Outline each blood parasite and name the species.
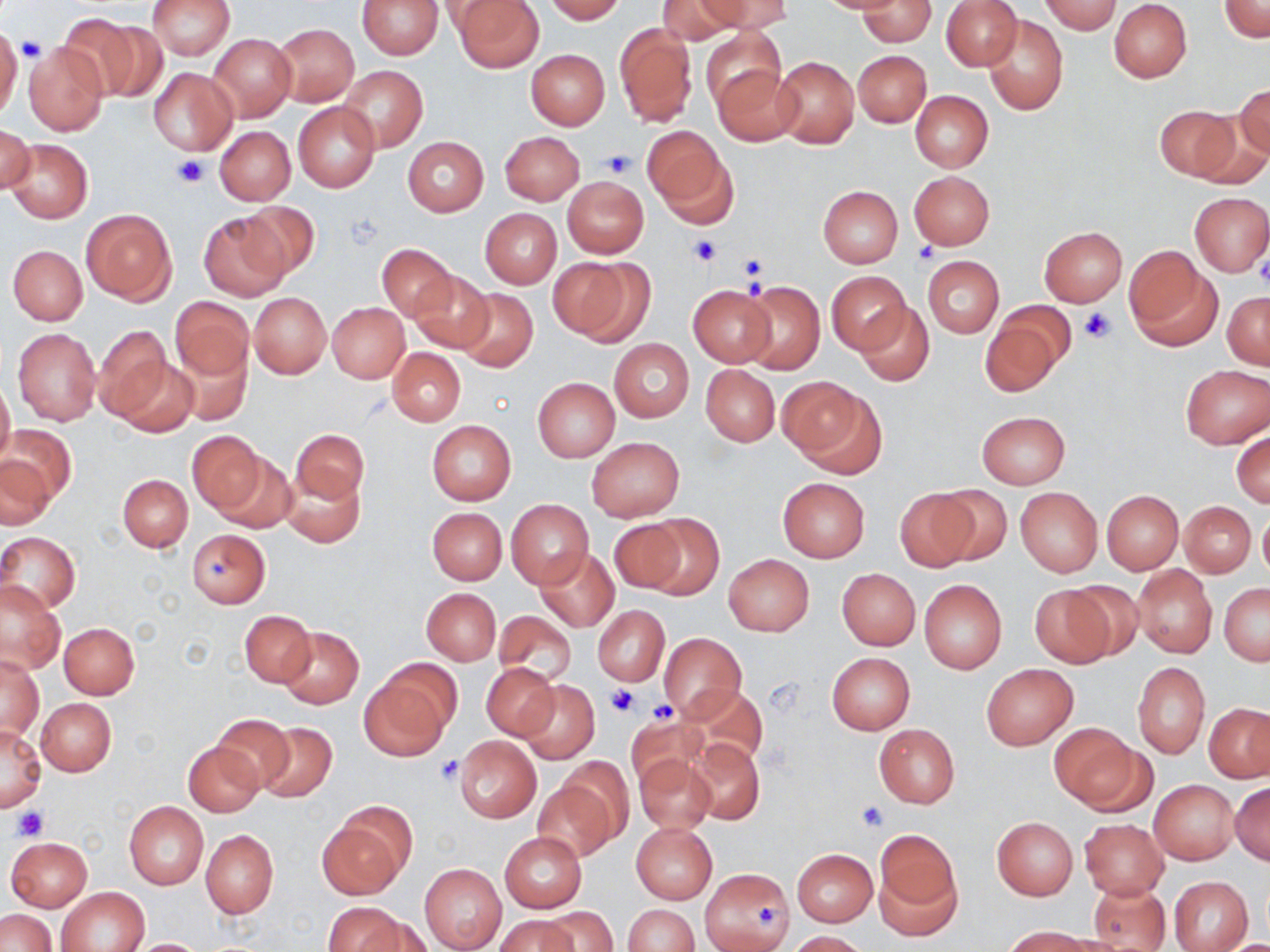

No blood parasites observed.

slide_level_diagnosis: negative for blood parasites
magnification: 1000x
stain: May-Grünwald-Giemsa
modality: light microscopy
image_size: 1270×952 pixels
uninfected_red_blood_cell_locations: 'approximate bounding boxes as [x1, y1, x2, y2] in pixels: [147, 0, 235, 59], [356, 0, 443, 59], [543, 0, 625, 22], [655, 0, 741, 44], [702, 0, 792, 34], [815, 0, 913, 15], [1041, 0, 1122, 35], [453, 1, 543, 71], [858, 1, 936, 48], [941, 1, 1021, 71], [1108, 1, 1193, 82], [1220, 1, 1269, 42], [57, 14, 144, 99], [982, 15, 1068, 116], [93, 23, 172, 101], [614, 23, 697, 126], [272, 24, 359, 105], [0, 26, 22, 119], [701, 26, 786, 113], [209, 34, 296, 121], [22, 43, 108, 136], [526, 49, 609, 129], [853, 50, 931, 127], [770, 54, 859, 150], [710, 64, 800, 146], [341, 66, 427, 152], [149, 68, 236, 153], [1234, 84, 1269, 163], [910, 90, 993, 173], [293, 102, 379, 192], [1154, 105, 1241, 181], [1, 125, 33, 196], [215, 126, 296, 205], [641, 127, 729, 220], [499, 131, 583, 205], [402, 137, 488, 216], [5, 138, 92, 223], [909, 171, 994, 249], [562, 176, 649, 258], [818, 185, 902, 267], [1189, 193, 1270, 276], [236, 200, 320, 281], [81, 208, 177, 306], [480, 208, 561, 287], [198, 212, 288, 300], [1038, 226, 1127, 307], [377, 243, 455, 322], [8, 245, 87, 325], [1125, 250, 1221, 351], [923, 256, 1004, 338], [557, 257, 654, 347], [408, 269, 495, 354], [827, 270, 910, 354], [738, 280, 825, 375], [686, 284, 777, 368], [455, 288, 538, 371], [1223, 291, 1270, 369], [249, 293, 331, 378], [169, 297, 253, 380], [855, 302, 933, 386], [328, 303, 410, 382], [981, 306, 1068, 394], [92, 324, 171, 420], [12, 327, 101, 426], [609, 339, 694, 421], [171, 341, 253, 423], [387, 347, 465, 425], [114, 357, 200, 438], [700, 365, 779, 447], [1180, 365, 1269, 448], [533, 377, 619, 461], [777, 377, 875, 462], [0, 379, 14, 471], [976, 409, 1071, 489], [427, 421, 517, 506], [3, 424, 75, 507], [293, 428, 369, 505], [1232, 428, 1269, 508], [187, 431, 265, 514], [587, 437, 684, 522], [215, 452, 298, 535], [0, 455, 53, 530], [281, 468, 364, 548], [118, 474, 193, 552], [778, 477, 869, 562], [934, 485, 1011, 564], [1016, 487, 1102, 576], [893, 489, 980, 572], [1101, 490, 1183, 574], [507, 499, 592, 588], [1180, 502, 1255, 576], [427, 506, 506, 584], [1258, 508, 1270, 583], [638, 514, 724, 596], [609, 518, 685, 593], [185, 528, 271, 608], [0, 531, 81, 613], [534, 546, 620, 632], [723, 554, 813, 636], [1132, 565, 1217, 659], [836, 568, 920, 649], [919, 578, 1007, 674], [1, 581, 65, 673], [1063, 581, 1144, 661], [1219, 584, 1270, 666], [1028, 585, 1118, 667], [421, 588, 500, 665], [594, 606, 669, 685], [240, 610, 315, 688], [495, 612, 577, 686], [491, 621, 579, 749], [58, 622, 139, 699], [278, 626, 364, 708], [659, 634, 746, 718], [827, 652, 914, 734], [1, 653, 42, 741], [384, 658, 464, 738], [482, 663, 558, 741], [981, 663, 1077, 750], [1133, 663, 1209, 758], [358, 672, 452, 762], [519, 680, 598, 763], [681, 684, 769, 768], [36, 698, 116, 776], [1205, 701, 1270, 782], [627, 713, 708, 791], [211, 714, 295, 792], [256, 722, 337, 801], [1049, 723, 1143, 811], [0, 725, 44, 811], [874, 725, 959, 807], [453, 736, 540, 823], [687, 739, 764, 824], [183, 742, 264, 817], [634, 753, 716, 835], [559, 757, 635, 838], [534, 779, 617, 861], [1150, 780, 1238, 864], [1230, 783, 1270, 865], [124, 801, 208, 889], [318, 813, 408, 899], [992, 817, 1078, 899], [1080, 819, 1167, 898], [630, 821, 717, 904], [201, 830, 278, 919], [873, 831, 961, 935], [500, 832, 585, 912], [6, 836, 92, 911], [792, 848, 877, 926], [419, 863, 506, 951], [701, 867, 794, 952], [1168, 875, 1253, 951], [1088, 879, 1172, 951], [55, 887, 151, 952], [321, 902, 407, 952], [624, 904, 698, 952], [538, 906, 616, 952], [0, 909, 57, 951], [496, 915, 576, 952], [1005, 926, 1090, 951], [789, 931, 869, 952], [125, 938, 210, 951]'
platelet_locations: 'approximate bounding boxes as [x1, y1, x2, y2] in pixels: [17, 36, 46, 63], [601, 148, 635, 176], [172, 154, 208, 189], [689, 235, 720, 265], [910, 243, 939, 268], [737, 253, 768, 285], [1079, 309, 1113, 343], [606, 683, 640, 718], [646, 698, 677, 725], [434, 757, 463, 785], [857, 799, 890, 831], [12, 804, 47, 841], [751, 896, 783, 934]'
field_of_view: one of a larger specimen
preparation: thin blood smear